State which parasite is depicted.
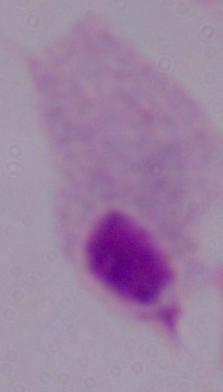

This is a trichomonad.

Summary:
  - Magnification: 1000x
  - Modality: micrograph